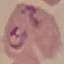

Result: malaria parasites detected. Acquired by smartphone through the microscope eyepiece. Cell patch, automatically extracted from a larger field of view and resized to 64 × 64 pixels. Giemsa stain. Thin blood smear.